Locate every Plasmodium parasite.
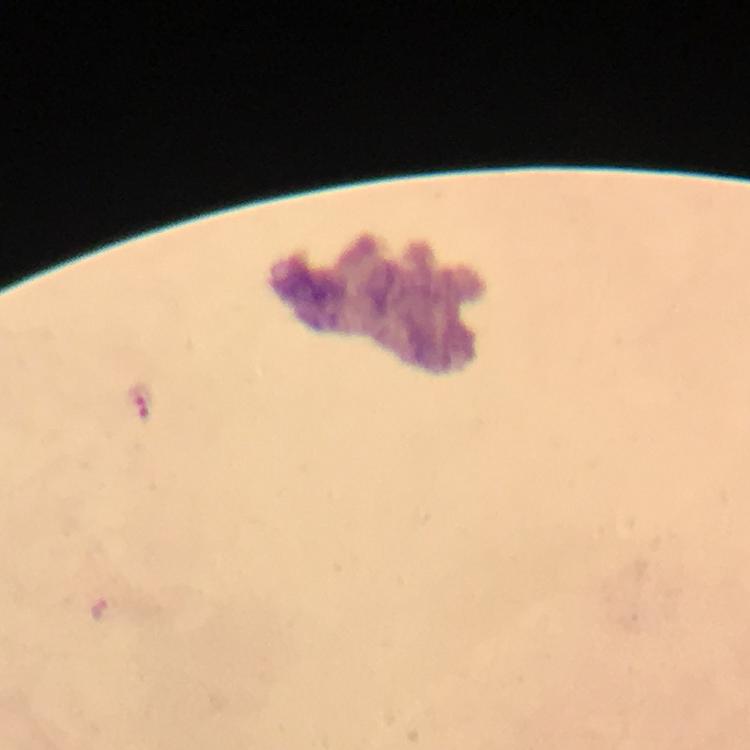

Approximate centers as [x, y] in pixels.
Plasmodium parasites: [140, 400].

Summary:
  - Stain: Giemsa
  - Context: from a diagnostic examination for malaria
  - Immersion oil: applied
  - Preparation: thick smear
  - Capture: smartphone mounted on the microscope
  - Magnification: 100x
  - Cropped from: a single field of view
  - Image size: 750×750 pixels